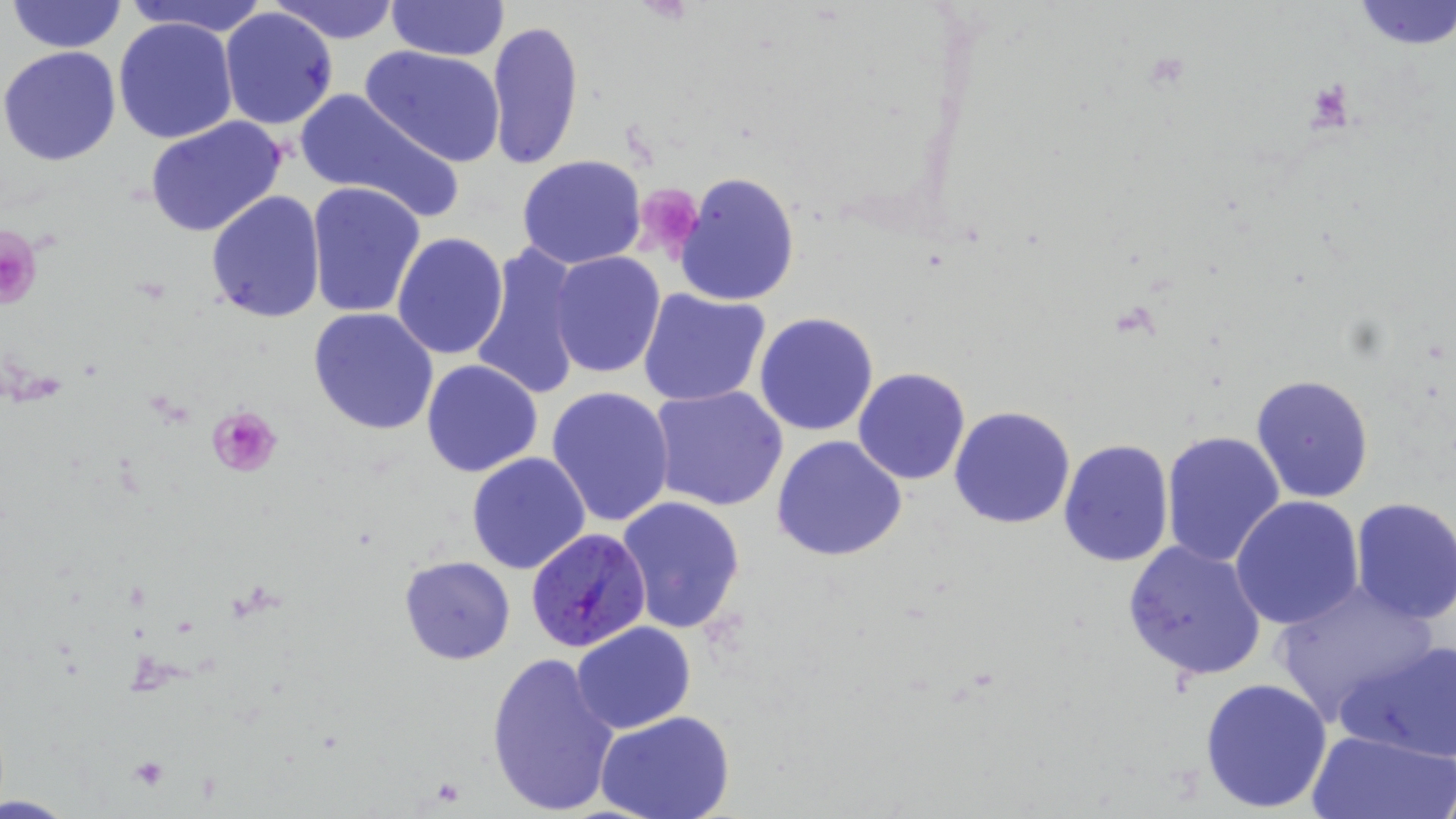

Approximate bounding boxes as (x1, y1, x2, y2) in pixels. Plasmodium falciparum-infected red blood cell locations: (526, 526, 653, 652). Platelet locations: (1307, 78, 1355, 129), (633, 183, 703, 256), (0, 226, 44, 312), (207, 406, 283, 476). Uninfected red blood cell locations: (6, 0, 126, 54), (125, 0, 274, 36), (272, 0, 403, 44), (386, 0, 509, 62), (1351, 1, 1456, 50), (218, 8, 338, 130), (113, 16, 239, 145), (485, 20, 584, 170), (0, 45, 123, 166), (361, 45, 508, 167), (292, 87, 461, 221), (145, 117, 288, 239), (516, 154, 648, 269), (673, 172, 802, 306), (305, 182, 428, 320), (205, 190, 326, 323), (391, 232, 509, 358), (471, 244, 584, 401), (551, 252, 666, 377), (637, 286, 771, 408), (641, 301, 879, 420), (308, 307, 439, 434), (754, 312, 878, 436), (421, 359, 543, 477), (853, 366, 971, 485), (1250, 373, 1376, 504), (546, 385, 676, 528), (648, 386, 789, 512), (950, 407, 1076, 529), (1160, 431, 1285, 567), (771, 435, 908, 562), (1058, 440, 1176, 568), (466, 452, 592, 574), (617, 495, 746, 634), (1231, 495, 1364, 630), (1350, 497, 1456, 623), (1121, 539, 1267, 682), (398, 555, 516, 665), (1271, 578, 1439, 727), (571, 622, 694, 734), (1339, 638, 1456, 763), (487, 650, 621, 818), (1198, 677, 1331, 814), (596, 712, 734, 819), (1305, 727, 1453, 819). Slide-level diagnosis: Plasmodium falciparum. Optical microscopy. May-Grünwald-Giemsa stain. Single field of view. Image is 1456×819 pixels. Thin blood film. 1000x magnification.